Describe the morphology of the red blood cells.
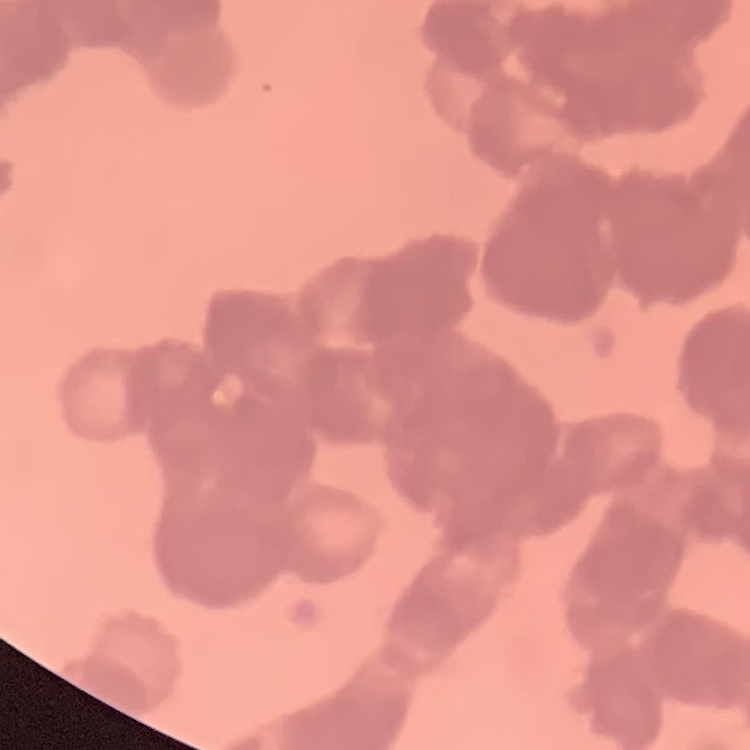
Rouleaux formation.

Summary:
  - Image type: square crop of a larger photomicrograph
  - Preparation: thin peripheral smear
  - Stain: Field's or Giemsa